State which cell type is depicted.
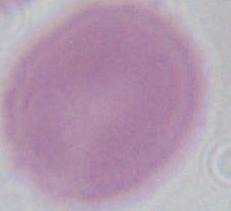

An erythrocyte.

modality: micrograph
magnification: 1000x